Locate every Plasmodium falciparum parasite and give its life-cycle stage, and locate every leukocyte and any debris.
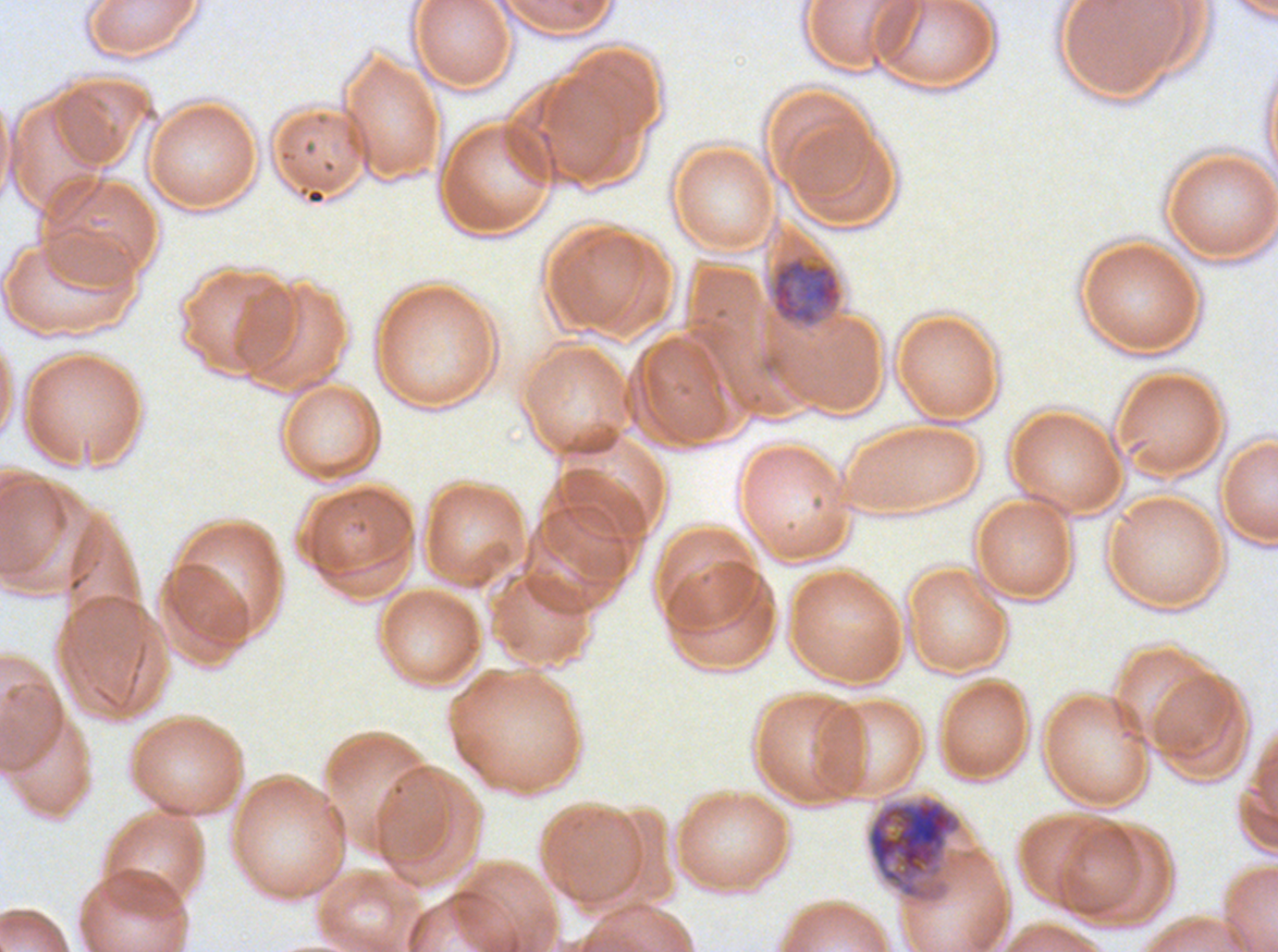

Approximate bounding boxes as [x1, y1, x2, y2] in pixels.
Mid trophozoites: [770, 254, 842, 326].
Late schizonts: [866, 795, 964, 904].
No rings, late-ring/early-trophozoite forms, late trophozoites, early schizonts, segmenters, gametocytes, leukocytes, or debris observed.

Summary:
  - Stain: Giemsa
  - Life-cycle stages observed: mid trophozoite, late schizont
  - Specimen: ex-vivo Plasmodium falciparum culture from a patient in The Gambia, grown for 24 to 48 hours
  - Image size: 1278×952 pixels
  - Field of view: one sub-image of a larger composite
  - Preparation: thin blood smear